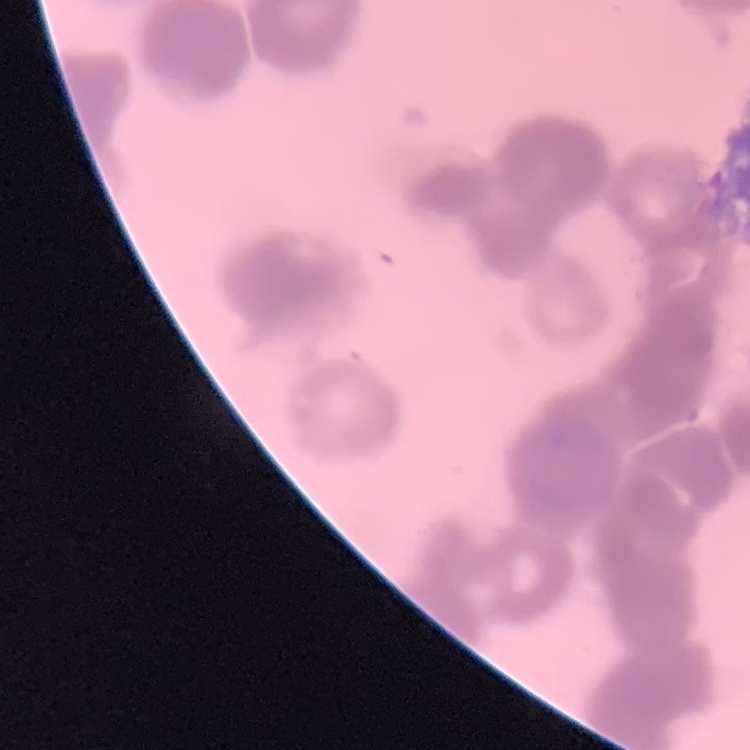
The red blood cells exhibit rouleaux formation. Thin peripheral smear. Stained with either Field's or Giemsa. Square crop of a larger photomicrograph.